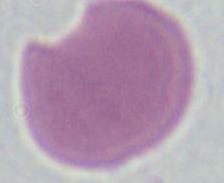
Summary:
  - Modality: micrograph
  - Identification: erythrocyte
  - Magnification: 1000x